Assess the morphology of the red blood cells.
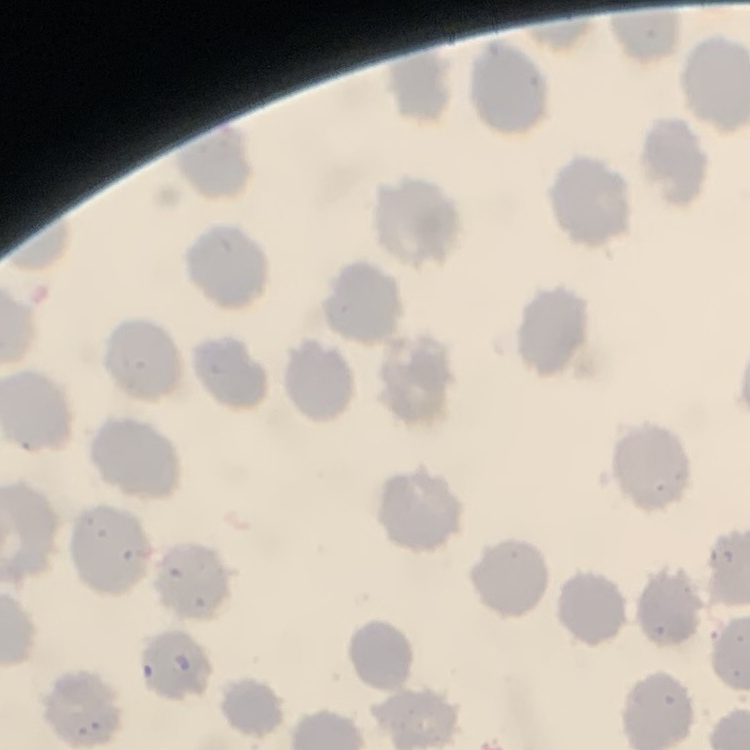
No rouleaux formation.

Summary:
  - Preparation: thin blood smear
  - Stain: Field's or Giemsa
  - Image type: one tile cut from a larger photomicrograph